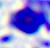
Summary:
  - Identification: white blood cell
  - Magnification: 400x
  - Modality: photomicrograph